Report the malaria status of this cell.
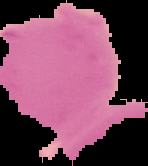

It is uninfected.

From a thin blood film. Segmented cell region on a black background. Image is 148×166 pixels.